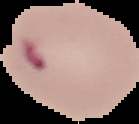

Malaria status: parasitized. From a thin blood film. The area outside the segmented cell region is set to black. Image is 139×124 pixels.